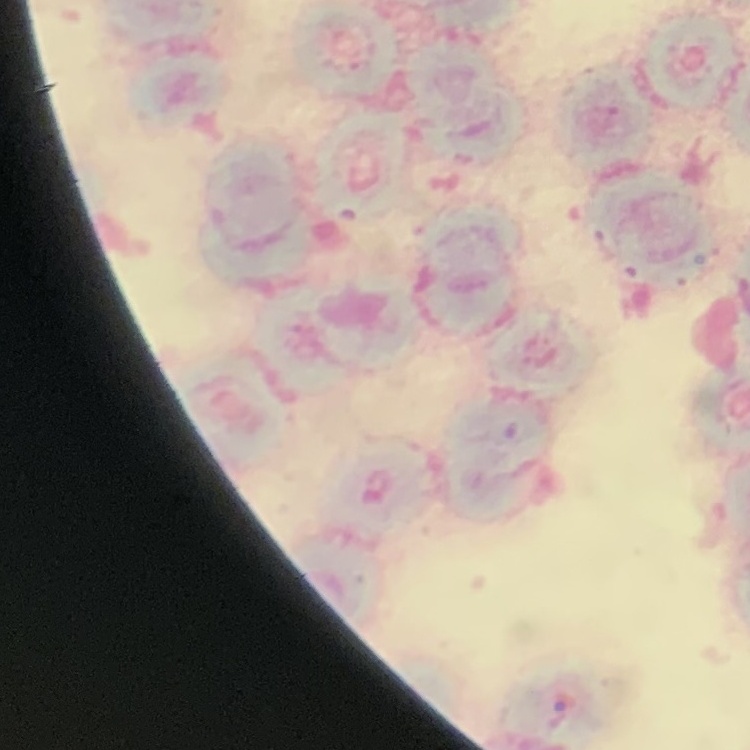
The red blood cells show rouleaux formation. Thin blood smear. Field's or Giemsa stain. One tile cut from a larger photomicrograph.